Report the malaria status of this cell.
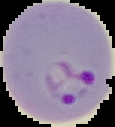

It is parasitized.

Segmented cell region on a black background. From a thin blood film. Image is 115×127 pixels.